Locate every Plasmodium falciparum-infected red blood cell.
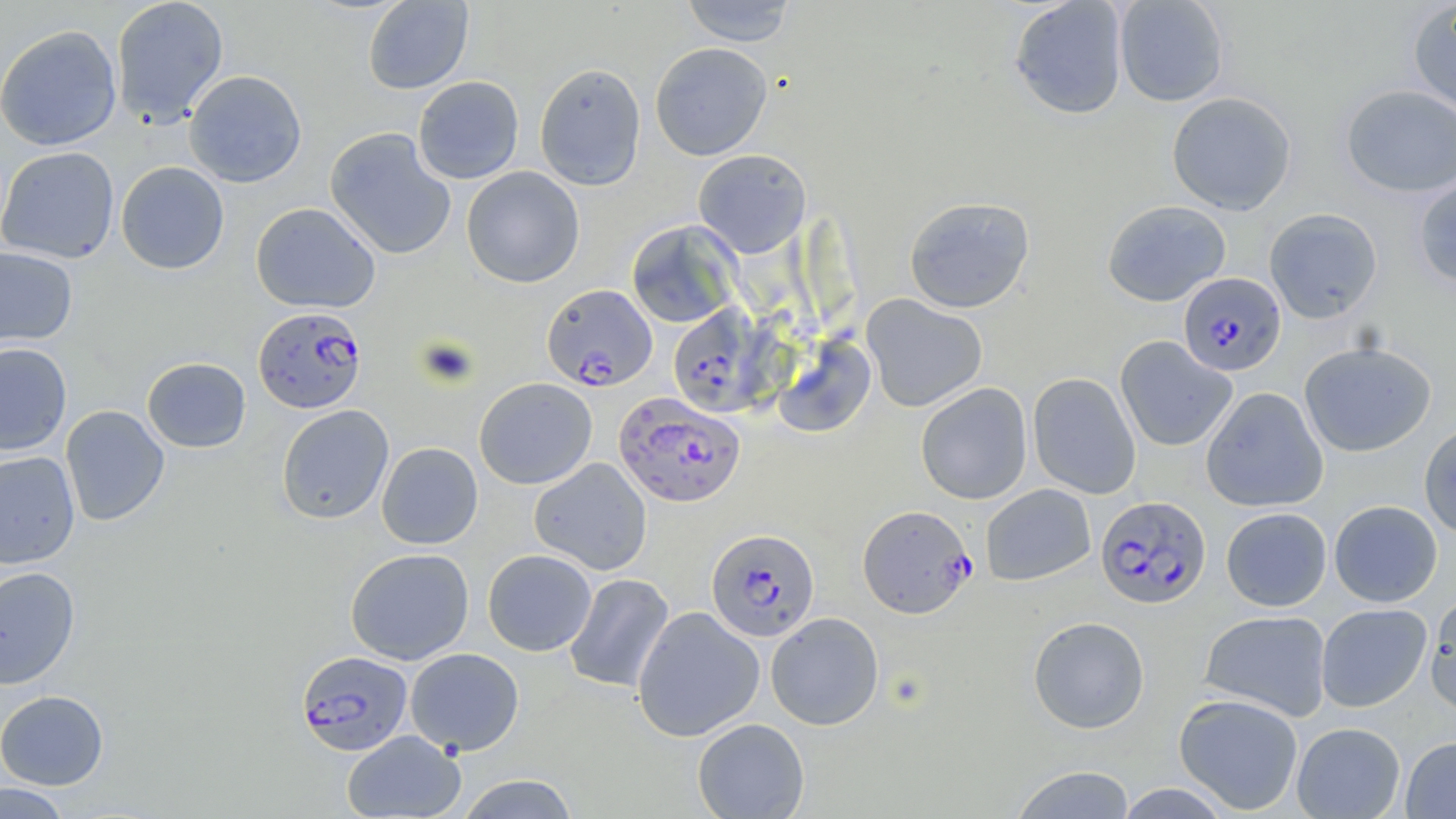
Approximate bounding boxes as (x1,y1)-(x2,y2) corner pairs in pixels.
Plasmodium falciparum-infected red blood cells: (1178,273)-(1286,376), (541,284)-(658,390), (668,304)-(772,417), (253,306)-(367,413), (614,393)-(745,507), (1095,495)-(1211,609), (857,504)-(975,618), (706,528)-(819,642), (296,650)-(413,756).

slide-level diagnosis = Plasmodium falciparum
preparation = thin blood smear
modality = light microscopy
stain = May-Grünwald-Giemsa
magnification = 1000x
field of view = single
image size = 1456×819 pixels
uninfected red blood cell locations = approximate bounding boxes as (x1,y1)-(x2,y2) corner pairs in pixels: (110,0)-(229,128), (362,0)-(473,94), (680,0)-(798,46), (1009,0)-(1128,119), (1114,0)-(1230,106), (1406,1)-(1456,121), (0,24)-(123,151), (650,43)-(773,161), (534,62)-(646,190), (184,69)-(307,188), (413,76)-(524,184), (1340,84)-(1456,197), (1167,92)-(1297,215), (325,127)-(456,260), (0,145)-(120,263), (693,149)-(811,258), (116,161)-(230,274), (461,166)-(585,288), (1413,174)-(1456,288), (904,196)-(1035,314), (1102,199)-(1231,306), (250,202)-(381,314), (1264,208)-(1383,323), (626,220)-(742,328), (0,246)-(78,347), (861,294)-(988,412), (772,333)-(876,438), (1115,336)-(1237,452), (1299,340)-(1436,457), (0,342)-(72,455), (142,357)-(251,452), (1028,372)-(1141,499), (474,377)-(597,490), (916,383)-(1032,504), (1201,386)-(1328,512), (60,405)-(169,527), (276,405)-(394,525), (1418,422)-(1456,540), (376,442)-(483,549), (0,451)-(80,568), (529,457)-(652,575), (981,484)-(1095,585), (1329,500)-(1443,606), (1221,507)-(1332,611), (345,548)-(474,665), (483,549)-(596,656), (0,566)-(81,690), (564,573)-(675,694), (1425,592)-(1456,719), (1316,603)-(1432,712), (632,606)-(765,742), (1199,609)-(1333,721), (766,612)-(884,730), (1028,615)-(1149,733), (405,648)-(524,755), (0,690)-(109,789), (1173,693)-(1303,814), (692,718)-(810,819), (1291,722)-(1406,818), (342,729)-(466,819), (1401,736)-(1456,818), (1009,765)-(1137,818), (455,773)-(581,818), (0,782)-(71,819), (1113,783)-(1236,819)